Identify the parasite.
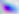

Toxoplasma gondii.

Captured at 400x magnification. Photomicrograph.